Classify this cell by malaria status.
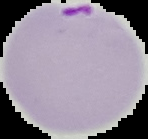
It is parasitized.

Summary:
  - Image type: segmented cell region with the area outside set to black
  - Image size: 148×139 pixels
  - Preparation: thin blood film